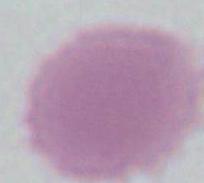
modality = photomicrograph
identification = erythrocyte
magnification = 1000x